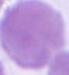
Summary:
  - Modality: photomicrograph
  - Identification: red blood cell
  - Magnification: 1000x